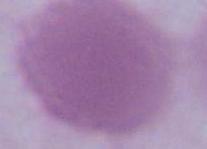
Micrograph. Captured at 1000x magnification. An erythrocyte is shown.